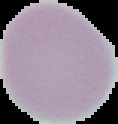

Summary:
  - Image size: 118×124 pixels
  - Malaria status: uninfected
  - Preparation: thin blood film
  - Image type: cell region segmented out of the field of view; surrounding area masked to black